Locate every Plasmodium parasite.
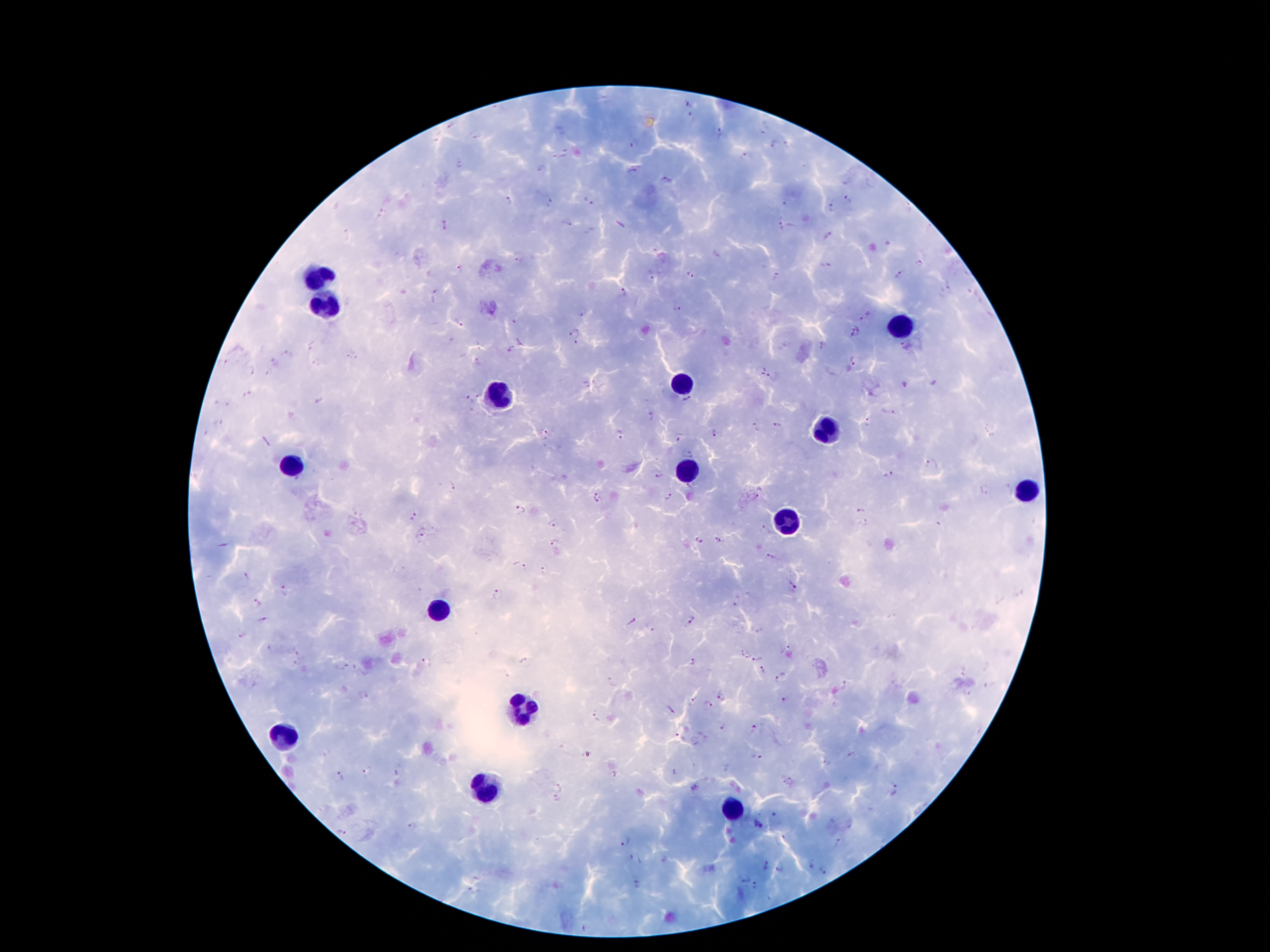
Approximate object centers, in pixels from the top-left corner.
Plasmodium parasites: (x=687, y=104), (x=693, y=118), (x=476, y=134), (x=719, y=134), (x=634, y=143), (x=774, y=144), (x=788, y=144), (x=565, y=154), (x=745, y=157), (x=459, y=164), (x=542, y=170), (x=632, y=171), (x=666, y=180), (x=848, y=197), (x=510, y=201), (x=588, y=201), (x=551, y=203), (x=784, y=203), (x=834, y=206), (x=567, y=223), (x=443, y=224), (x=780, y=226), (x=829, y=236), (x=519, y=258), (x=919, y=261), (x=824, y=264), (x=460, y=267), (x=688, y=275), (x=900, y=276), (x=776, y=278), (x=652, y=280), (x=948, y=285), (x=624, y=293), (x=435, y=294), (x=677, y=310), (x=582, y=311), (x=866, y=316), (x=516, y=321), (x=459, y=324), (x=855, y=331), (x=576, y=332), (x=521, y=341), (x=577, y=344), (x=312, y=345), (x=822, y=346), (x=906, y=346), (x=512, y=350), (x=285, y=356), (x=351, y=356), (x=479, y=360), (x=273, y=361), (x=854, y=361), (x=222, y=363), (x=252, y=368), (x=761, y=372), (x=774, y=377), (x=585, y=384), (x=904, y=384), (x=248, y=395), (x=477, y=396), (x=469, y=399), (x=320, y=401), (x=688, y=401), (x=229, y=403), (x=887, y=412), (x=652, y=416), (x=219, y=421), (x=869, y=422), (x=780, y=425), (x=755, y=427), (x=715, y=432), (x=620, y=433), (x=680, y=435), (x=689, y=453), (x=932, y=464), (x=889, y=474), (x=659, y=477), (x=451, y=487), (x=759, y=492), (x=668, y=496), (x=598, y=499), (x=861, y=509), (x=519, y=510), (x=414, y=515), (x=937, y=524), (x=553, y=525), (x=423, y=533), (x=765, y=533), (x=718, y=539), (x=699, y=541), (x=554, y=545), (x=770, y=557), (x=520, y=564), (x=543, y=570), (x=246, y=578), (x=791, y=585), (x=284, y=591), (x=498, y=594), (x=257, y=600), (x=735, y=602), (x=263, y=619), (x=692, y=620), (x=630, y=621), (x=652, y=628), (x=758, y=628), (x=241, y=636), (x=270, y=647), (x=786, y=649), (x=298, y=651), (x=740, y=652), (x=747, y=655), (x=759, y=659), (x=692, y=661), (x=427, y=663), (x=523, y=663), (x=344, y=667), (x=763, y=670), (x=778, y=680), (x=845, y=684), (x=363, y=694), (x=720, y=694), (x=692, y=701), (x=784, y=701), (x=709, y=704), (x=671, y=711), (x=597, y=716), (x=723, y=727), (x=753, y=730), (x=678, y=737), (x=851, y=755), (x=758, y=759), (x=828, y=763), (x=366, y=770), (x=677, y=772), (x=397, y=773), (x=614, y=776), (x=338, y=777), (x=786, y=781), (x=559, y=787), (x=897, y=791), (x=556, y=800), (x=776, y=814), (x=411, y=824), (x=758, y=825), (x=342, y=831), (x=625, y=843), (x=840, y=843), (x=631, y=858), (x=765, y=866), (x=811, y=866), (x=823, y=870), (x=780, y=871), (x=746, y=881), (x=637, y=884), (x=755, y=886), (x=473, y=890), (x=586, y=927).

{
  "field_of_view": "single",
  "capture": "smartphone through the microscope eyepiece",
  "image_size": "1270×952 pixels",
  "patient_malaria_status": "positive for Plasmodium falciparum",
  "magnification": "100x",
  "preparation": "thick blood smear",
  "stain": "Giemsa",
  "leukocyte_locations": "approximate object centers, in pixels from the top-left corner: (x=319, y=278), (x=323, y=305), (x=897, y=321), (x=682, y=381), (x=495, y=395), (x=821, y=434), (x=288, y=467), (x=688, y=471), (x=1024, y=489), (x=786, y=526), (x=440, y=608), (x=522, y=709), (x=284, y=735), (x=483, y=789), (x=733, y=811)"
}